Comment on the morphology of the red blood cells.
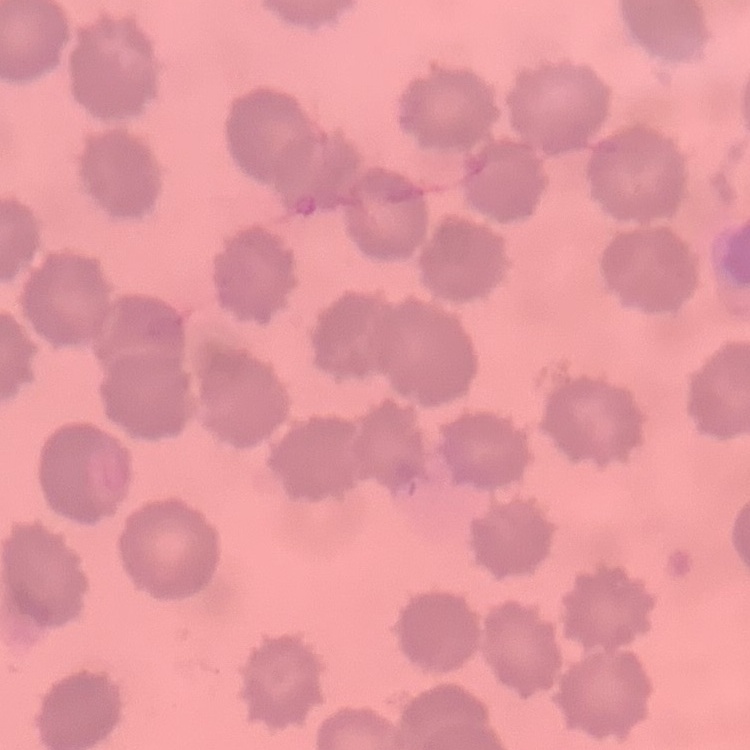

No rouleaux formation.

Thin blood film. One tile cut from a larger photomicrograph. Stained with either Field's or Giemsa.